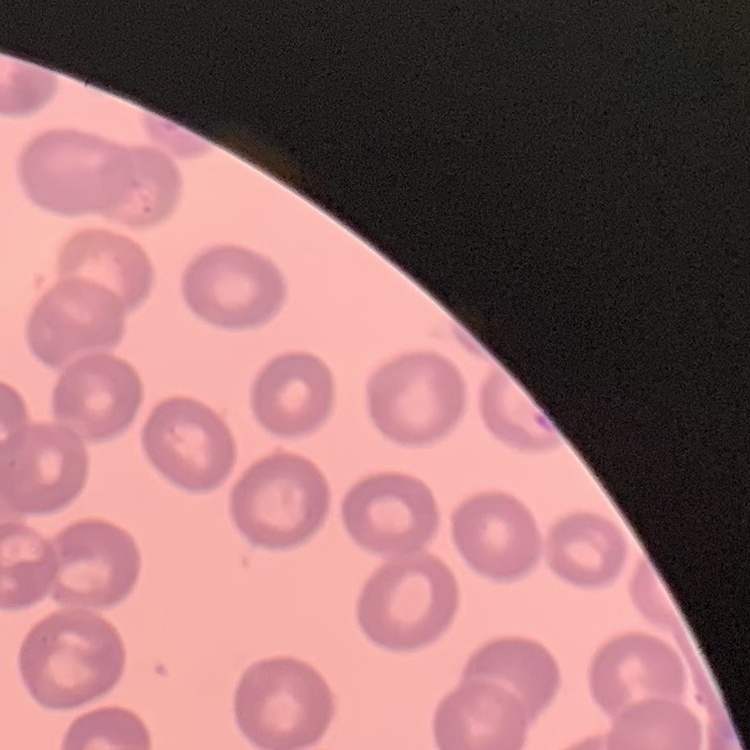

Summary:
  - Red blood cell morphology: no rouleaux formation
  - Stain: Field's or Giemsa
  - Image type: square crop of a larger photomicrograph
  - Preparation: thin blood smear